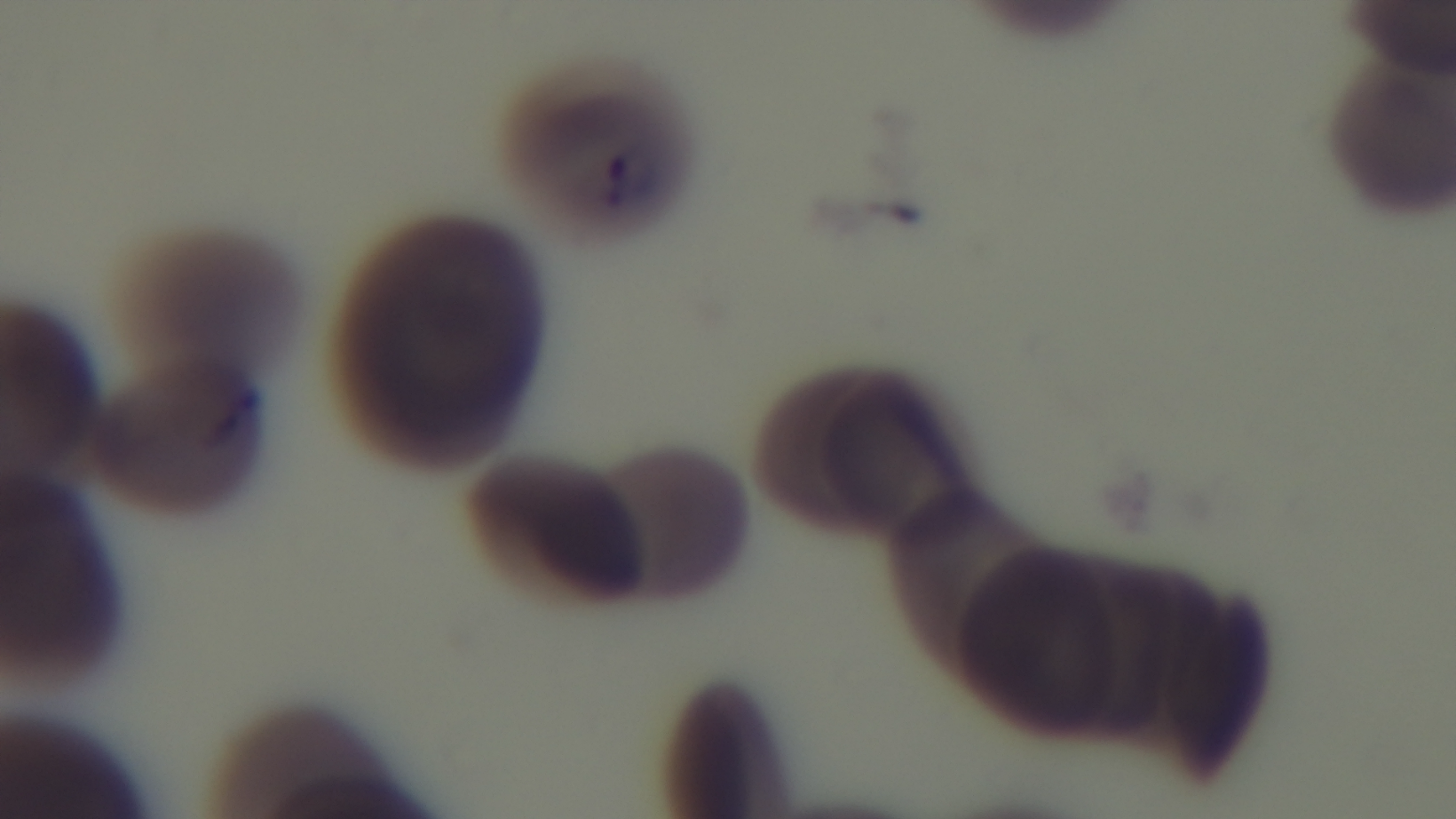
objective: 100x oil immersion
capture: mounted 4K digital camera
field_of_view: one from the slide
modality: light microscopy
preparation: thin
malaria_status: infected
stain: Giemsa